State which parasite is depicted.
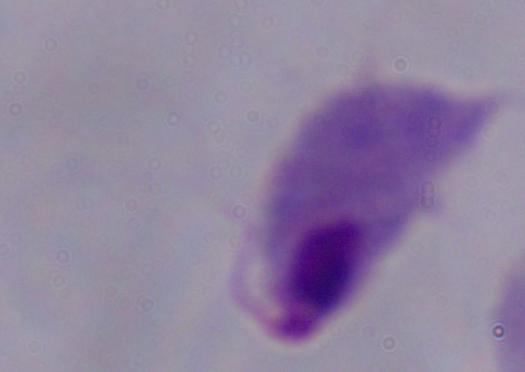

This is a trichomonad.

magnification = 1000x
modality = micrograph